Name the blood parasite species.
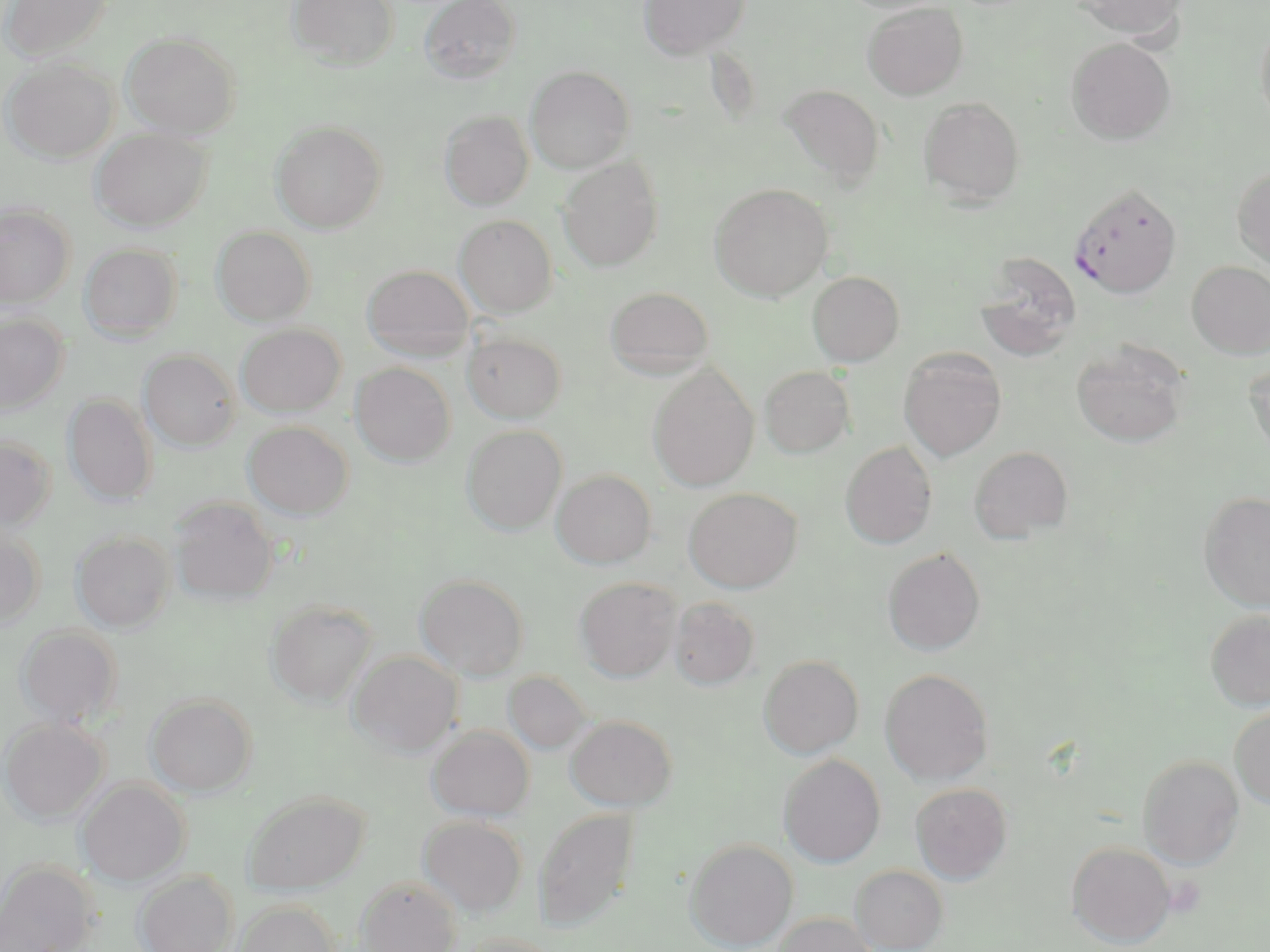

Plasmodium falciparum.

stain = May-Grünwald-Giemsa
Plasmodium falciparum-infected red blood cell locations = approximate bounding boxes as (x1,y1)-(x2,y2) corner pairs in pixels: (1070,183)-(1182,298)
uninfected red blood cell locations = approximate bounding boxes as (x1,y1)-(x2,y2) corner pairs in pixels: (1,0)-(112,62), (287,0)-(399,71), (420,0)-(521,84), (639,0)-(750,59), (1071,0)-(1188,39), (862,2)-(968,100), (1255,17)-(1270,130), (122,32)-(241,138), (1067,37)-(1175,145), (2,58)-(117,163), (526,66)-(634,173), (780,85)-(885,190), (918,96)-(1026,206), (439,111)-(533,210), (271,120)-(387,233), (92,127)-(211,232), (558,157)-(664,272), (1232,165)-(1270,269), (710,182)-(834,301), (0,203)-(75,308), (455,215)-(557,318), (211,226)-(316,326), (80,244)-(183,342), (973,252)-(1081,360), (1187,260)-(1270,359), (361,264)-(475,361), (806,270)-(904,366), (604,285)-(715,379), (0,312)-(69,413), (236,324)-(346,417), (463,332)-(566,423), (1071,342)-(1189,448), (898,348)-(1007,462), (139,350)-(241,451), (1244,358)-(1270,464), (350,363)-(455,466), (648,366)-(759,491), (759,366)-(855,458), (63,394)-(157,507), (243,421)-(353,519), (462,425)-(567,535), (0,435)-(56,531), (840,442)-(938,549), (968,446)-(1073,544), (552,469)-(657,569), (684,488)-(802,592), (1198,490)-(1270,612), (169,497)-(279,605), (0,527)-(45,629), (72,531)-(174,633), (882,547)-(986,656), (415,574)-(529,680), (575,576)-(681,682), (668,597)-(760,690), (267,599)-(377,707), (1204,609)-(1270,711), (15,625)-(124,728), (348,650)-(462,756), (759,655)-(864,758), (879,668)-(994,785), (503,671)-(593,756), (145,693)-(257,796), (1229,704)-(1270,810), (565,714)-(678,811), (1,717)-(108,825), (427,725)-(535,821), (779,754)-(886,867), (1137,755)-(1245,869), (76,779)-(190,887), (910,783)-(1013,884), (243,790)-(371,894), (534,808)-(638,930), (418,816)-(528,917), (685,838)-(798,951), (1066,841)-(1176,947), (0,862)-(98,952), (850,864)-(949,952), (133,870)-(238,952), (354,877)-(461,952), (233,900)-(341,952), (0,908)-(67,952), (772,912)-(879,952), (457,931)-(555,952)
platelet locations = approximate bounding boxes as (x1,y1)-(x2,y2) corner pairs in pixels: (1165,876)-(1206,918)
preparation = thin blood film
modality = optical microscopy
image size = 1270×952 pixels
field of view = one of a larger specimen
magnification = 1000x